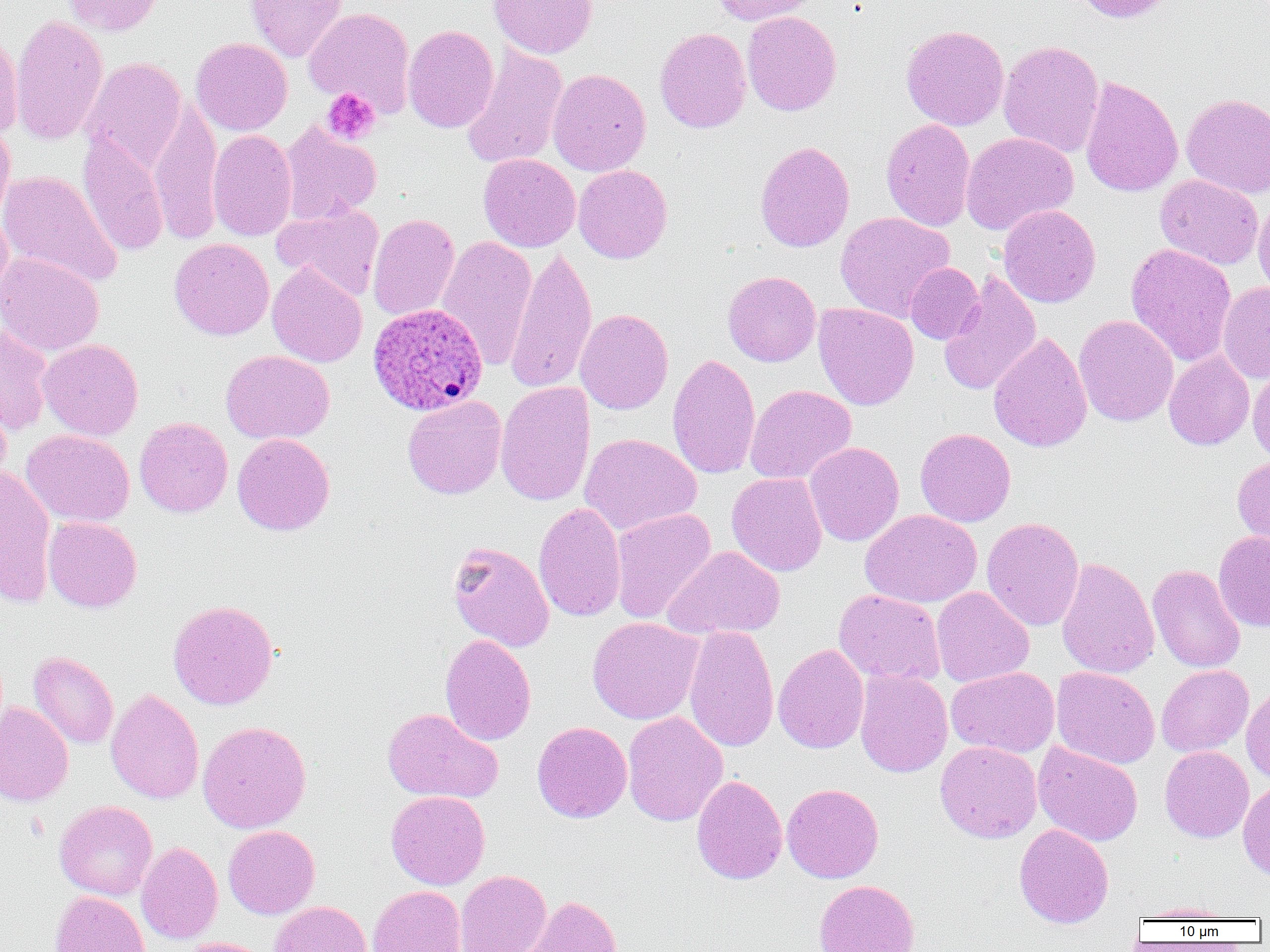

Summary:
  - Coordinate format: approximate bounding boxes as [x1, y1, x2, y2] in pixels
  - Uninfected red blood cell locations: [63, 0, 165, 36], [244, 0, 349, 62], [488, 0, 598, 59], [711, 0, 821, 25], [1071, 0, 1173, 23], [303, 6, 416, 116], [742, 11, 842, 116], [9, 13, 108, 146], [402, 25, 499, 133], [900, 25, 1009, 131], [654, 27, 751, 133], [0, 29, 23, 140], [190, 37, 292, 135], [998, 40, 1104, 158], [461, 43, 569, 170], [82, 57, 187, 174], [547, 68, 651, 177], [1080, 76, 1184, 198], [1181, 93, 1270, 198], [148, 100, 223, 245], [880, 118, 976, 231], [0, 119, 15, 227], [279, 121, 381, 225], [208, 129, 297, 241], [960, 132, 1078, 235], [77, 133, 169, 257], [754, 140, 855, 252], [479, 153, 580, 252], [573, 164, 673, 263], [0, 170, 123, 288], [1155, 175, 1264, 270], [1253, 199, 1270, 297], [273, 203, 384, 300], [998, 204, 1101, 308], [0, 211, 13, 306], [835, 211, 954, 321], [367, 213, 460, 321], [435, 235, 537, 370], [169, 238, 274, 340], [1126, 243, 1236, 366], [505, 246, 596, 394], [0, 253, 104, 357], [904, 262, 984, 344], [266, 263, 367, 367], [723, 271, 821, 367], [939, 271, 1042, 397], [1217, 281, 1270, 383], [813, 302, 919, 410], [575, 308, 674, 415], [1074, 314, 1178, 426], [0, 324, 54, 434], [988, 331, 1092, 453], [38, 339, 144, 441], [220, 349, 334, 444], [1163, 351, 1254, 451], [667, 353, 760, 480], [1248, 364, 1270, 462], [495, 381, 596, 506], [745, 384, 856, 485], [402, 395, 507, 499], [0, 399, 12, 495], [134, 417, 233, 517], [915, 427, 1016, 527], [21, 429, 135, 527], [232, 433, 335, 536], [579, 433, 701, 536], [804, 442, 904, 546], [1232, 453, 1270, 556], [0, 466, 56, 607], [727, 472, 827, 576], [533, 502, 626, 622], [610, 508, 717, 624], [860, 509, 982, 608], [43, 516, 142, 613], [981, 517, 1085, 631], [1213, 531, 1270, 632], [447, 540, 554, 652], [663, 545, 785, 640], [1056, 557, 1159, 679], [1148, 564, 1246, 673], [931, 587, 1034, 688], [833, 589, 945, 686], [168, 599, 279, 710], [587, 617, 704, 725], [683, 625, 779, 752], [439, 633, 536, 746], [773, 643, 869, 754], [28, 650, 119, 750], [1156, 664, 1254, 757], [1051, 666, 1160, 769], [946, 667, 1059, 758], [854, 669, 952, 778], [1241, 683, 1270, 784], [105, 688, 204, 804], [0, 701, 74, 807], [382, 707, 503, 804], [622, 711, 728, 826], [197, 721, 311, 833], [532, 721, 632, 822], [935, 741, 1042, 843], [1033, 742, 1143, 846], [1160, 746, 1254, 842], [691, 774, 788, 884], [1238, 779, 1270, 882], [782, 783, 884, 883], [386, 790, 490, 889], [54, 800, 158, 900], [1013, 823, 1114, 928], [223, 825, 320, 919], [135, 841, 223, 944], [455, 870, 551, 952], [813, 880, 920, 952], [368, 885, 467, 952], [50, 890, 150, 952], [518, 894, 624, 952], [269, 900, 372, 952], [1133, 901, 1238, 921], [176, 937, 275, 952]
  - Plasmodium ovale-infected red blood cell locations: [367, 303, 488, 416]
  - Platelet locations: [322, 87, 381, 145]
  - Slide-level diagnosis: Plasmodium ovale
  - Magnification: 1000x
  - Field of view: one of a larger specimen
  - Image size: 1270×952 pixels
  - Preparation: thin blood film
  - Modality: optical microscopy